Locate every Plasmodium parasite and every leukocyte.
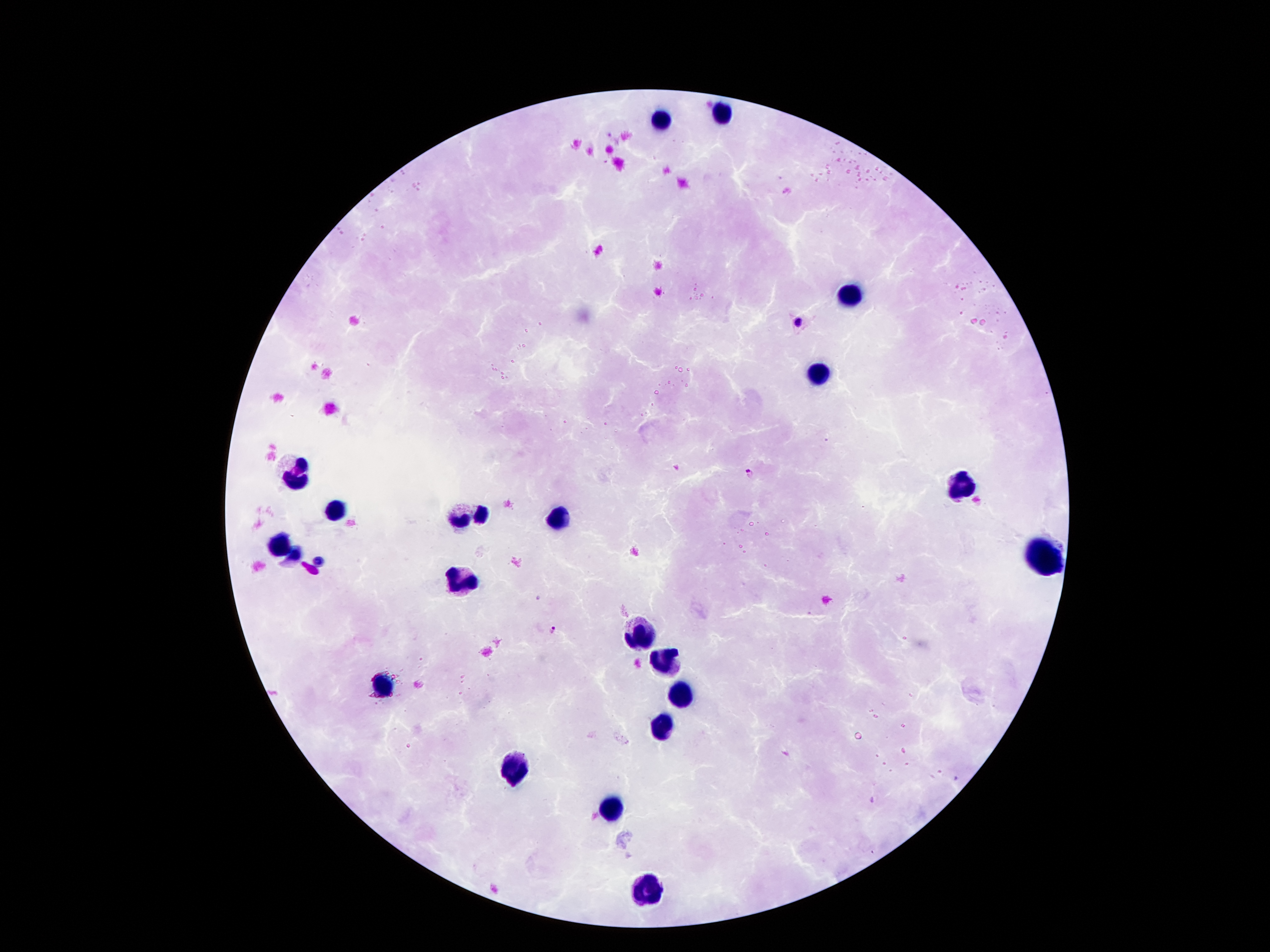

Approximate object centers, in pixels from the top-left corner.
Plasmodium parasites: (x=800, y=321), (x=748, y=473), (x=553, y=629).
Leukocytes: (x=723, y=113), (x=661, y=119), (x=847, y=296), (x=818, y=376), (x=298, y=473), (x=960, y=484), (x=337, y=510), (x=560, y=515), (x=472, y=518), (x=279, y=542), (x=1044, y=559), (x=464, y=581), (x=640, y=635), (x=668, y=663), (x=384, y=686), (x=679, y=694), (x=664, y=727), (x=513, y=766), (x=611, y=811), (x=648, y=891).

Single field of view. Smartphone photograph taken through the microscope eyepiece. Image is 1270×952 pixels. Thick peripheral-blood smear. 100x magnification. Patient malaria status: infected with Plasmodium falciparum. Giemsa-stained preparation.